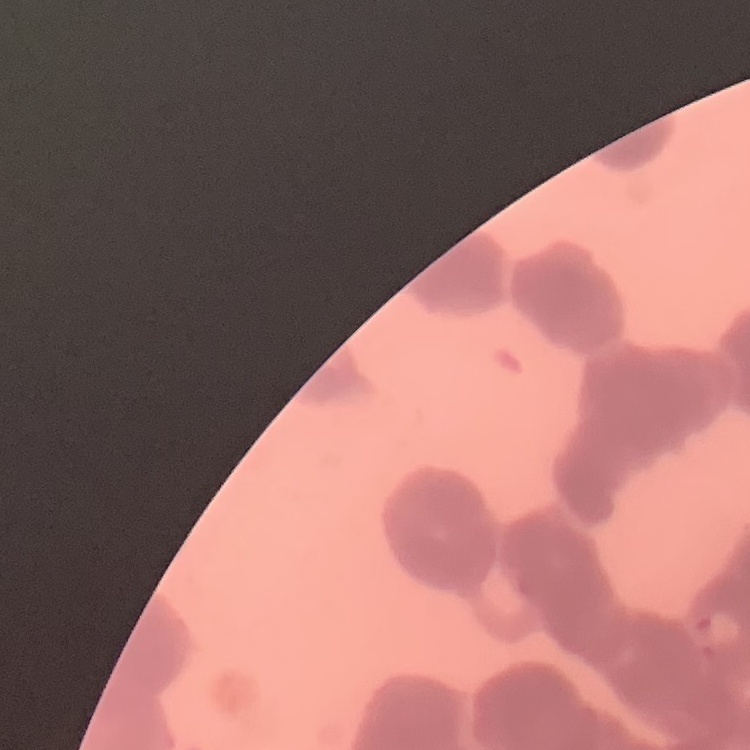
red_blood_cell_morphology: rouleaux formation
stain: Field's or Giemsa
image_type: one tile cut from a larger photomicrograph
preparation: thin peripheral smear